Give the position of every Plasmodium parasite.
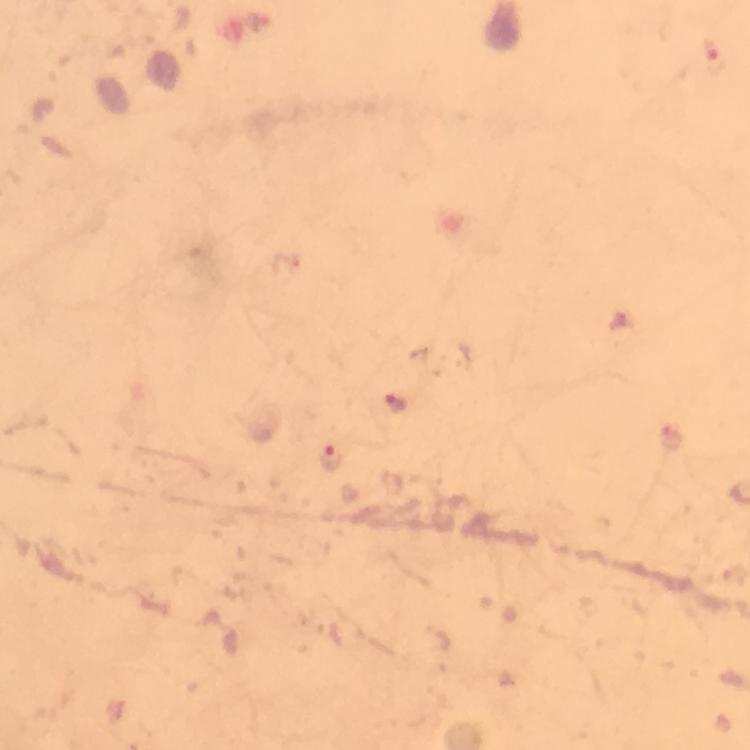
Approximate centers as {x, y} in pixels.
Plasmodium parasites: {396, 403}, {329, 456}.

Image is 750×750 pixels. From a malaria diagnostic workup. Smartphone photograph taken through a microscope. Giemsa stain. Cropped region of a single field of view. Immersion oil applied. 100x magnification. Thick blood film.